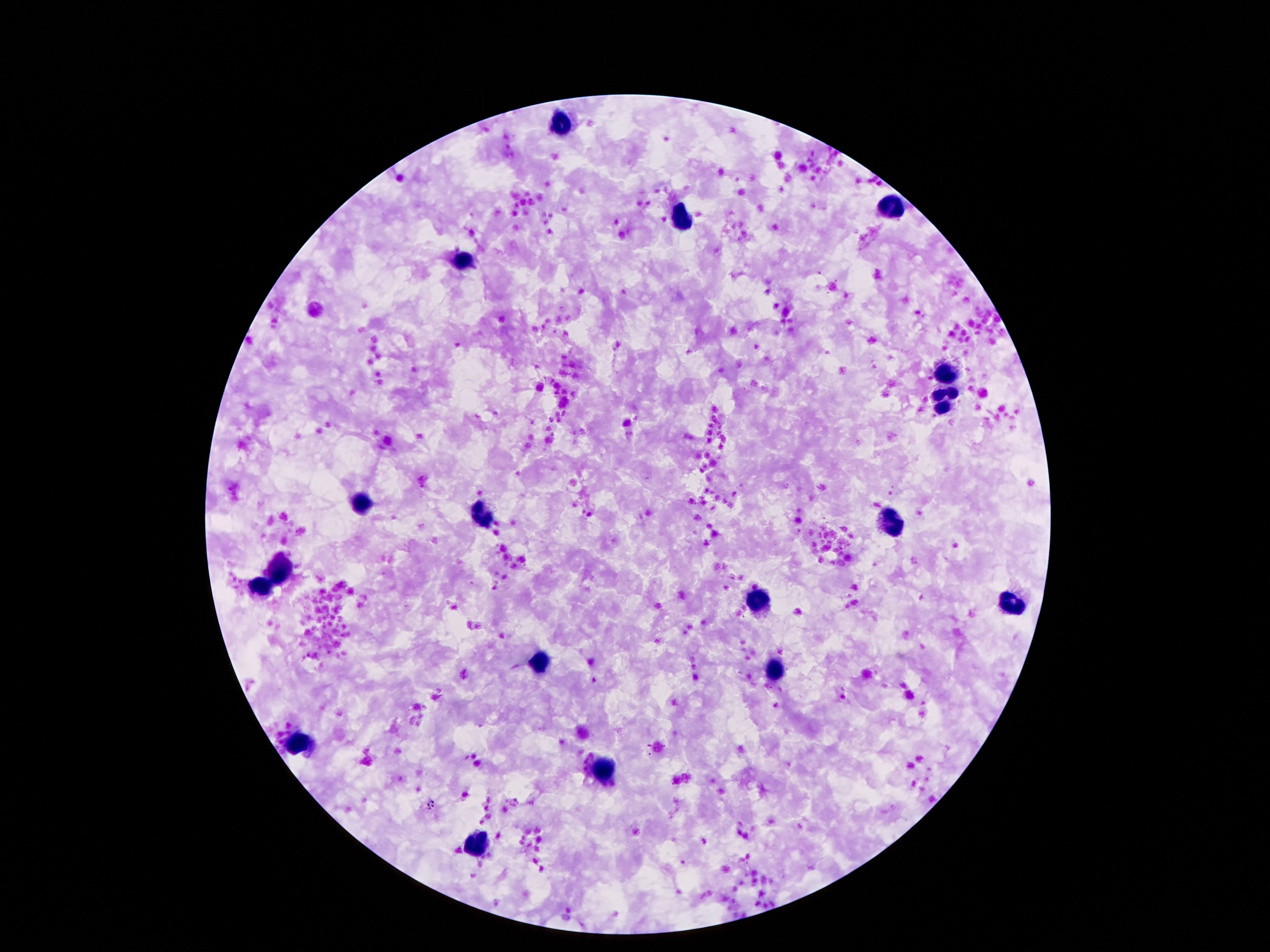

{
  "leukocyte_locations": "approximate object centers, in pixels from the top-left corner: (x=560, y=124), (x=891, y=207), (x=682, y=220), (x=461, y=261), (x=947, y=376), (x=947, y=401), (x=362, y=506), (x=480, y=514), (x=891, y=525), (x=282, y=573), (x=261, y=585), (x=759, y=600), (x=1011, y=605), (x=540, y=661), (x=776, y=669), (x=299, y=743), (x=607, y=767), (x=476, y=844)",
  "preparation": "thick peripheral-blood smear",
  "stain": "Giemsa",
  "field_of_view": "single",
  "capture": "smartphone camera through the microscope eyepiece",
  "image_size": "1270×952 pixels",
  "magnification": "100x",
  "patient_malaria_status": "uninfected"
}